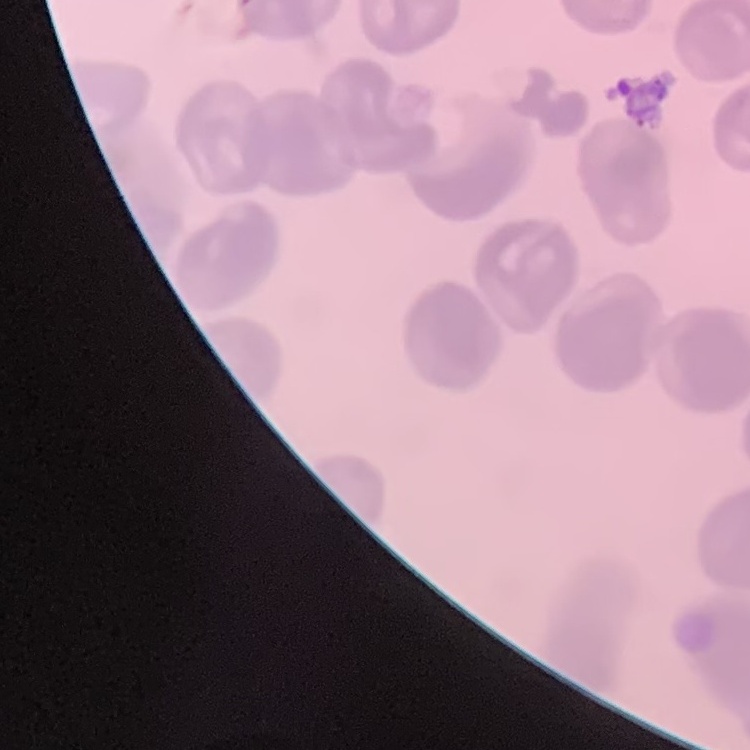
erythrocyte_morphology: no rouleaux formation
preparation: thin blood smear
image_type: square crop of a larger photomicrograph
stain: Field's or Giemsa